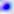
Summary:
  - Magnification: 400x
  - Identification: Toxoplasma gondii
  - Modality: photomicrograph